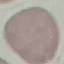

Summary:
  - Malaria status: uninfected
  - Capture: smartphone through the microscope eyepiece
  - Preparation: thin smear
  - Stain: Giemsa
  - Image type: automatically extracted cell patch, resized to 64 × 64 pixels